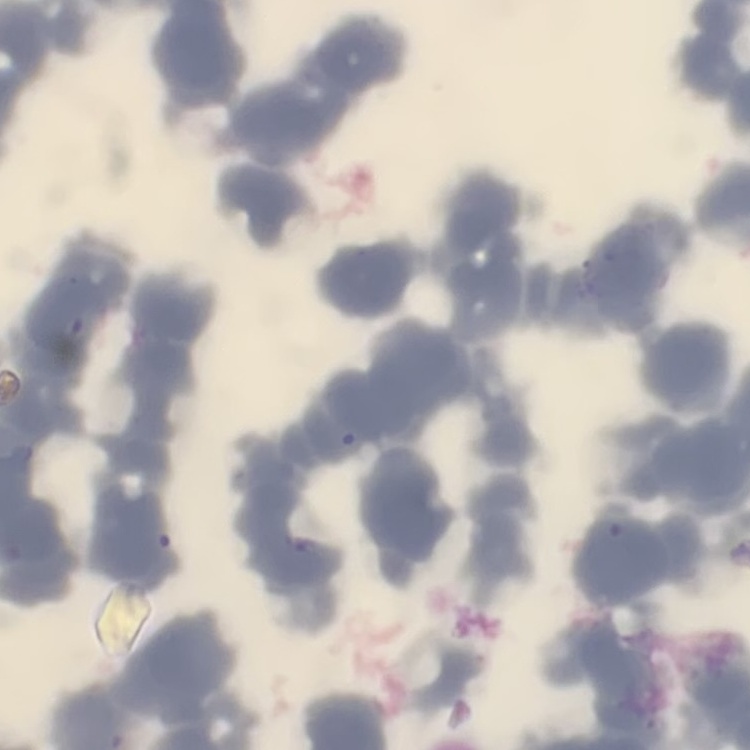
The red blood cells show rouleaux formation. Square crop of a larger photomicrograph. Stained with either Field's or Giemsa. Thin blood smear.